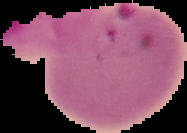

preparation = thin blood smear
image type = segmented cell region with the area outside set to black
result = malaria parasites identified
image size = 187×133 pixels